State the preparation type.
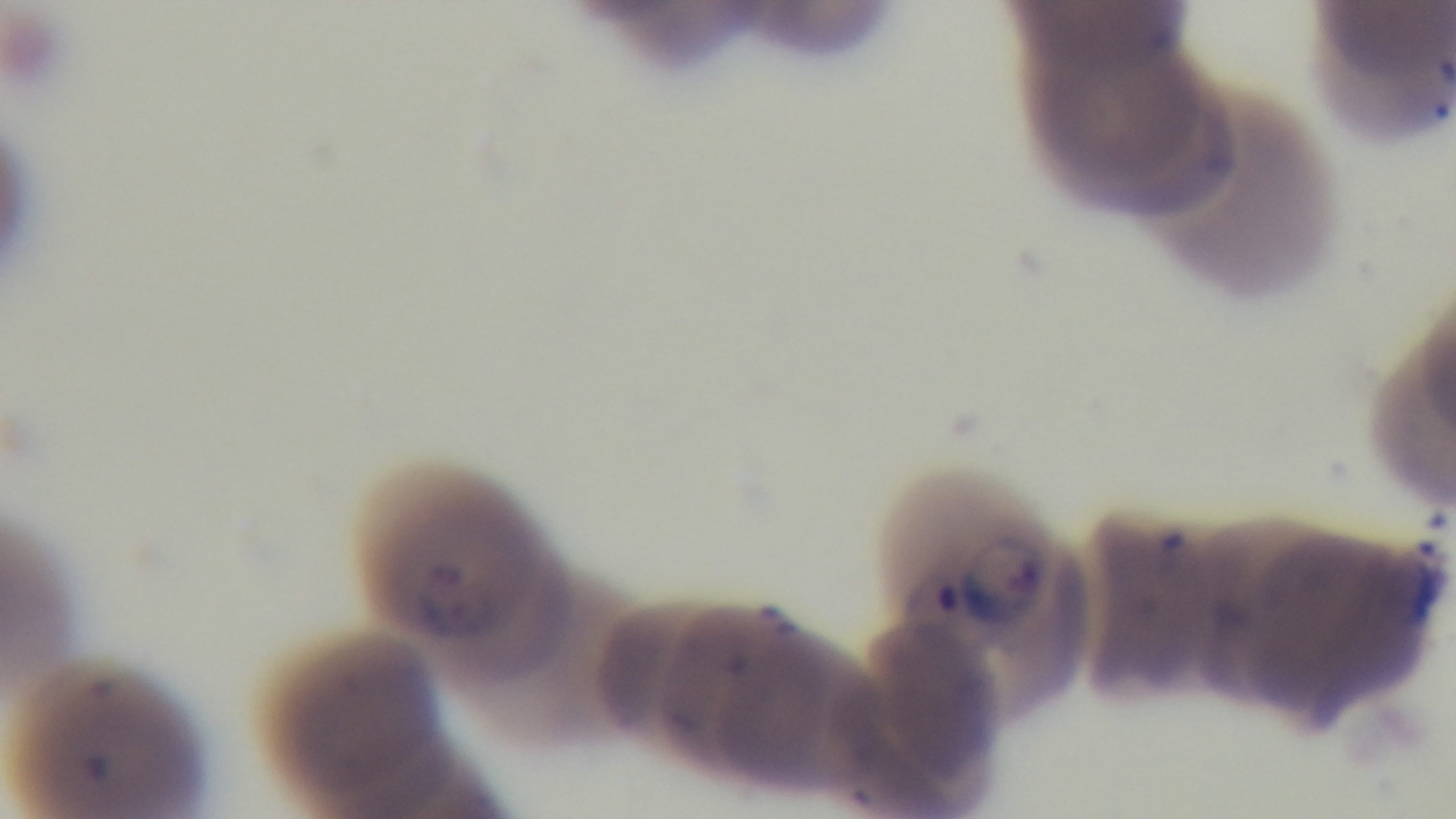
Thin.

capture: mounted 4K digital camera
stain: Giemsa
field_of_view: one from the slide
objective: 100x oil immersion
modality: light microscopy
malaria_status: positive